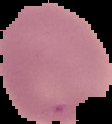

{
  "image_size": "112×124 pixels",
  "image_type": "segmented cell region on a black background",
  "malaria_status": "uninfected",
  "preparation": "thin blood smear"
}